Point out leukocytes.
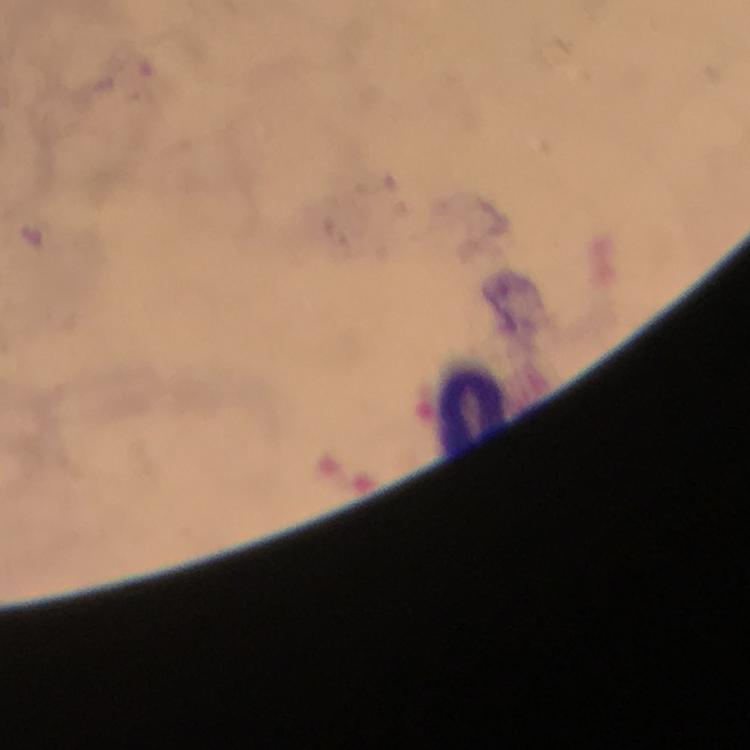

Approximate centers as (x, y) in pixels.
Leukocytes: (472, 412).

Giemsa stain. Malaria parasites: none seen. Cropped region of a single field of view. Thick blood smear. At 100x magnification. Image is 750×750 pixels. Photographed with a smartphone mounted on the microscope. From a malaria diagnostic workup. Immersion oil was used.